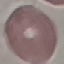 Result: no malaria parasites detected. Acquired by smartphone through the microscope eyepiece. Giemsa stain. Thin smear of blood. Automatically extracted cell patch, resized to 64 × 64 pixels.